Assess this cell for malaria.
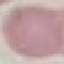
It is uninfected.

Acquired by smartphone through the microscope eyepiece. Thin smear of blood. Cell patch, automatically extracted from a larger field of view and resized to 64 × 64 pixels. Giemsa-stained preparation.